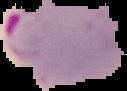
Summary:
  - Preparation: thin blood smear
  - Malaria status: parasitized
  - Image size: 127×91 pixels
  - Image type: cell region segmented out of the field of view; surrounding area masked to black